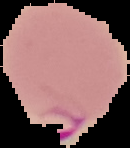

Result: malaria parasites detected. From a thin blood film. Cell region segmented out of the field of view; the surrounding area is masked to black. Image is 130×148 pixels.